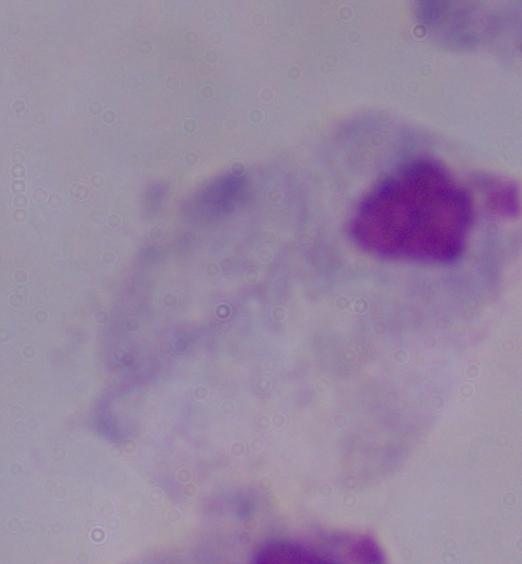
Summary:
  - Magnification: 1000x
  - Identification: trichomonad
  - Modality: micrograph